Outline each uninfected red blood cell.
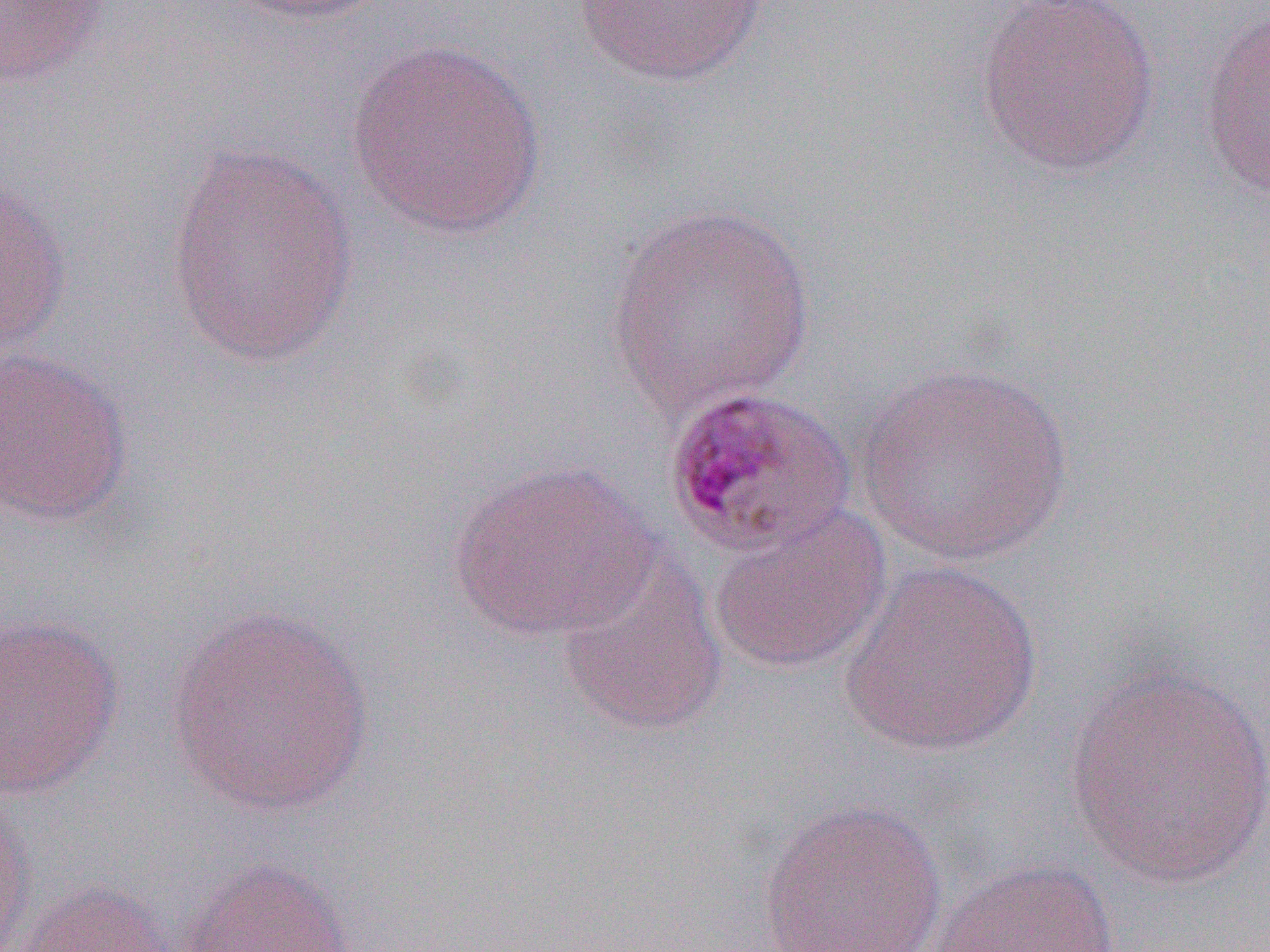

Approximate bounding boxes as (x1,y1)-(x2,y2) corner pairs in pixels.
Uninfected red blood cells: (224,0)-(394,26), (571,0)-(775,86), (973,0)-(1161,179), (0,1)-(115,87), (1198,9)-(1270,201), (345,37)-(548,238), (166,142)-(361,369), (0,174)-(71,359), (604,204)-(816,416), (0,346)-(135,528), (856,361)-(1074,566), (445,458)-(660,643), (707,503)-(892,676), (555,551)-(729,738), (840,561)-(1044,758), (165,605)-(376,817), (0,614)-(125,800), (1060,663)-(1270,890), (0,795)-(35,951), (756,799)-(948,952), (178,857)-(358,952), (926,858)-(1120,952), (16,877)-(178,952).

Slide-level diagnosis: Plasmodium malariae. Thin blood smear. 1000x magnification. Single field of view. Light microscopy. Image is 1270×952 pixels.